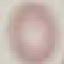

result = negative for malaria parasites
capture = smartphone through the microscope eyepiece
stain = Giemsa
preparation = thin blood smear
image type = automatically extracted cell patch, resized to 64 × 64 pixels